Assess the morphology of the red blood cells.
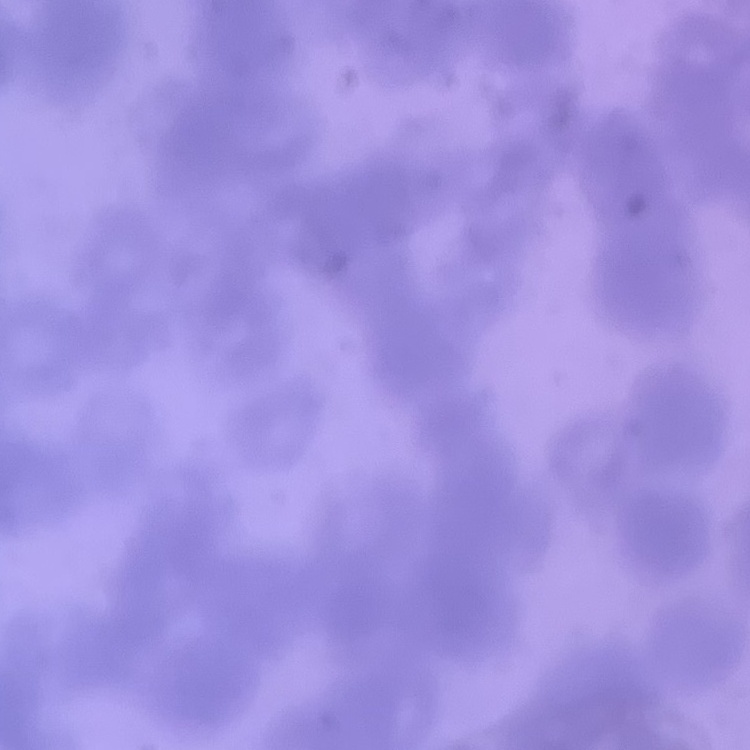

They show rouleaux formation.

Thin blood film. Stained with either Field's or Giemsa. Square crop of a larger photomicrograph.